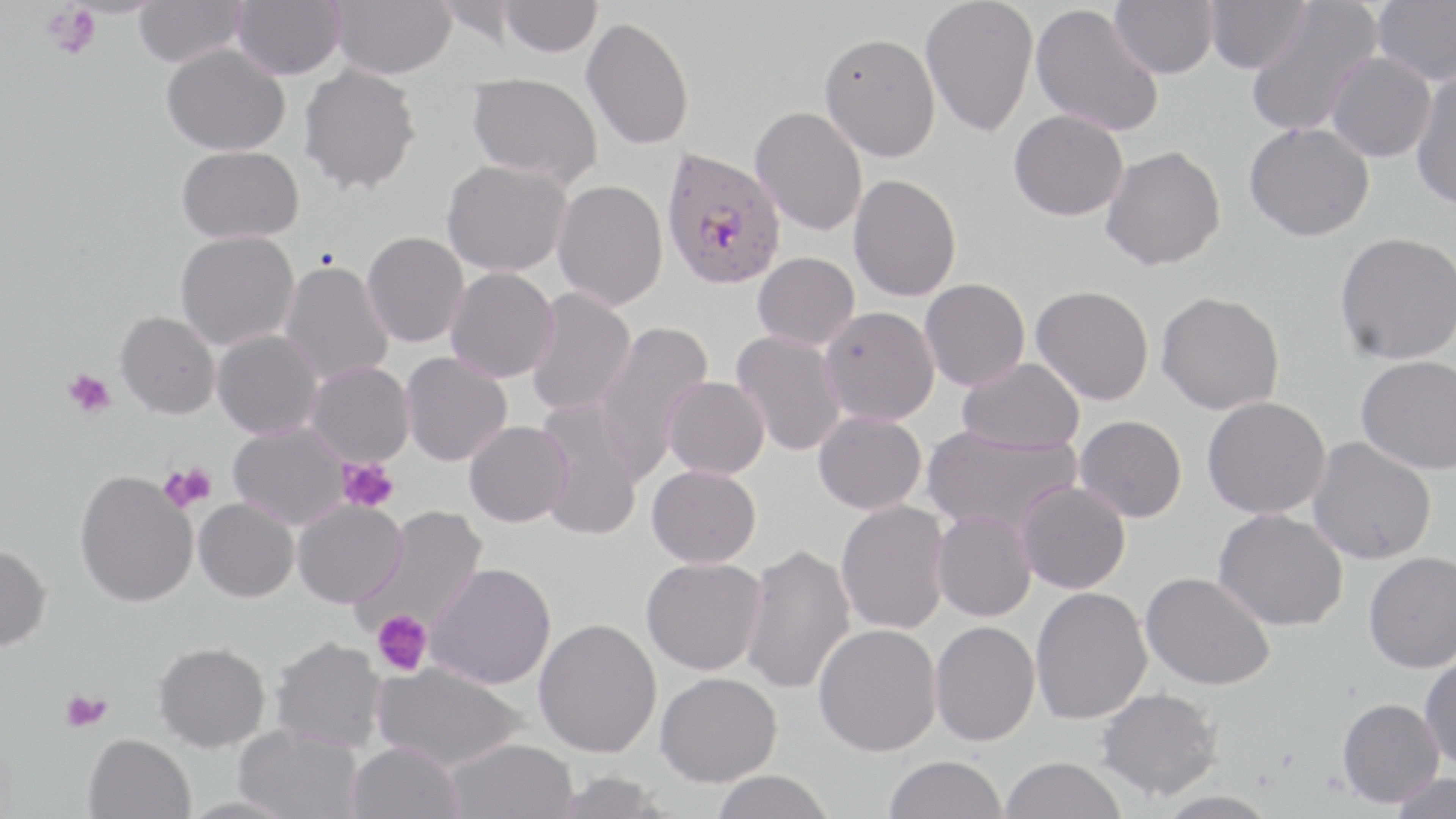
Summary:
  - Coordinate format: approximate bounding boxes as (x1,y1)-(x2,y2) corner pairs in pixels
  - Platelet locations: (42,3)-(100,60), (62,368)-(116,419), (338,458)-(399,513), (158,462)-(215,513), (372,609)-(432,677), (60,690)-(111,732)
  - Plasmodium falciparum-infected red blood cell locations: (659,145)-(786,291)
  - Uninfected red blood cell locations: (134,0)-(248,67), (231,0)-(345,79), (329,0)-(456,79), (433,0)-(524,46), (499,0)-(602,57), (920,0)-(1039,138), (1110,0)-(1217,79), (1205,0)-(1310,74), (1372,0)-(1456,87), (1244,1)-(1383,138), (1031,3)-(1163,137), (581,16)-(694,150), (820,32)-(940,161), (161,43)-(290,155), (1326,51)-(1437,162), (298,63)-(421,196), (1411,69)-(1456,211), (467,73)-(602,187), (750,106)-(867,236), (1008,109)-(1129,221), (1244,122)-(1374,241), (1100,145)-(1226,270), (177,146)-(304,243), (442,159)-(572,277), (848,173)-(961,301), (552,180)-(667,311), (175,230)-(299,351), (362,231)-(469,348), (1334,231)-(1456,365), (753,252)-(859,350), (279,259)-(394,387), (445,267)-(558,383), (920,278)-(1030,391), (1031,285)-(1153,405), (524,287)-(636,418), (1156,290)-(1284,415), (819,306)-(940,425), (115,311)-(220,418), (593,321)-(714,479), (212,329)-(323,439), (731,330)-(847,457), (401,352)-(512,467), (1355,354)-(1456,473), (957,358)-(1084,454), (305,362)-(414,467), (663,377)-(769,480), (1202,396)-(1331,519), (534,399)-(645,541), (813,410)-(927,515), (1074,415)-(1187,522), (465,420)-(572,527), (227,421)-(351,530), (921,424)-(1082,536), (1307,436)-(1437,565), (647,464)-(761,568), (75,470)-(198,607), (1015,480)-(1130,594), (194,498)-(299,602), (292,499)-(406,609), (836,500)-(950,635), (355,506)-(488,637), (1212,508)-(1348,631), (931,510)-(1036,622), (741,542)-(855,696), (0,544)-(51,652), (1363,551)-(1456,673), (641,557)-(767,676), (425,563)-(556,689), (1140,571)-(1275,690), (1030,586)-(1152,725), (533,618)-(661,758), (930,620)-(1040,746), (813,623)-(942,757), (271,637)-(388,753), (153,643)-(271,752), (1419,652)-(1456,771), (372,661)-(528,773), (655,672)-(782,787), (1096,687)-(1223,800), (1337,697)-(1444,807), (232,722)-(363,818), (83,733)-(196,819), (444,738)-(578,819), (346,742)-(463,819), (884,755)-(1008,819), (999,756)-(1127,818), (710,770)-(835,819), (554,771)-(670,818), (1389,772)-(1455,819), (1155,790)-(1279,819)
  - Slide-level diagnosis: Plasmodium falciparum
  - Image size: 1456×819 pixels
  - Modality: light microscopy
  - Preparation: thin blood smear
  - Field of view: single
  - Magnification: 1000x
  - Stain: May-Grünwald-Giemsa